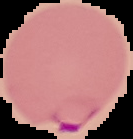

{
  "image_size": "133×139 pixels",
  "preparation": "thin blood film",
  "malaria_status": "parasitized",
  "image_type": "segmented cell region on a black background"
}